Report the malaria status of this cell.
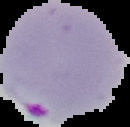
Parasitized.

Summary:
  - Preparation: thin blood smear
  - Image type: segmented cell region on a black background
  - Image size: 130×127 pixels